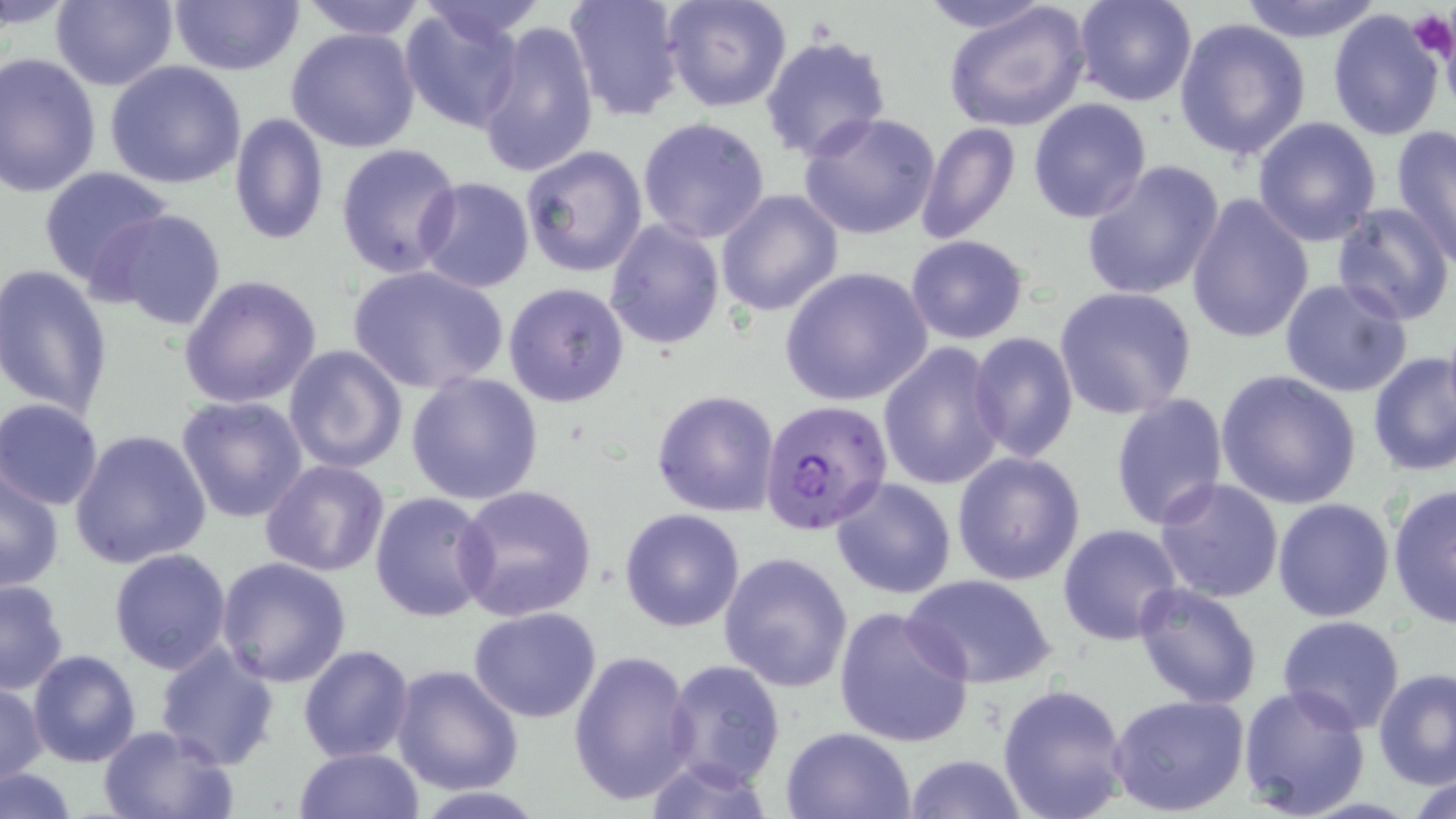

slide_level_diagnosis: Plasmodium falciparum
uninfected_red_blood_cell_locations: 'approximate bounding boxes as [x1, y1, x2, y2] in pixels: [52, 0, 178, 91], [294, 0, 432, 42], [415, 0, 549, 42], [563, 0, 687, 122], [662, 0, 793, 113], [912, 0, 1057, 36], [1074, 0, 1198, 107], [1235, 0, 1385, 40], [168, 1, 305, 76], [944, 2, 1091, 134], [398, 4, 527, 133], [1327, 7, 1447, 141], [476, 18, 599, 178], [1173, 18, 1313, 162], [287, 27, 420, 154], [760, 34, 890, 161], [0, 51, 102, 199], [104, 60, 247, 191], [1027, 98, 1152, 223], [228, 111, 331, 245], [799, 112, 942, 241], [636, 117, 771, 245], [1253, 117, 1383, 246], [916, 120, 1021, 247], [1390, 123, 1456, 265], [335, 143, 461, 278], [520, 145, 649, 277], [1081, 160, 1226, 303], [38, 165, 174, 294], [415, 178, 535, 293], [715, 188, 843, 317], [1185, 193, 1314, 344], [1330, 200, 1456, 326], [94, 208, 230, 334], [604, 219, 725, 352], [905, 234, 1031, 345], [347, 264, 510, 395], [0, 265, 115, 419], [777, 265, 934, 408], [177, 274, 322, 411], [1279, 278, 1412, 397], [503, 282, 631, 409], [1054, 287, 1198, 418], [969, 331, 1079, 466], [877, 343, 1006, 492], [282, 345, 408, 473], [1368, 351, 1454, 479], [1217, 370, 1361, 508], [405, 371, 545, 505], [651, 391, 779, 518], [1109, 393, 1229, 531], [177, 396, 308, 522], [0, 399, 103, 510], [0, 405, 191, 528], [70, 429, 211, 569], [951, 452, 1086, 585], [259, 459, 389, 578], [1, 468, 65, 593], [831, 477, 957, 601], [1153, 478, 1284, 603], [1387, 483, 1455, 631], [454, 485, 597, 622], [369, 491, 497, 625], [1273, 497, 1395, 621], [619, 508, 746, 631], [1058, 524, 1183, 645], [109, 549, 233, 675], [719, 551, 855, 692], [214, 556, 352, 686], [902, 574, 1057, 688], [0, 579, 70, 696], [1132, 584, 1263, 710], [832, 606, 974, 748], [468, 607, 602, 723], [1276, 616, 1406, 735], [153, 643, 281, 770], [298, 644, 415, 764], [568, 649, 696, 807], [27, 650, 141, 767], [661, 658, 787, 791], [391, 662, 524, 796], [1372, 668, 1456, 790], [0, 683, 46, 788], [996, 683, 1132, 819], [1238, 684, 1370, 817], [1109, 692, 1251, 816], [97, 725, 236, 819], [779, 725, 917, 818], [294, 744, 423, 819], [904, 752, 1028, 819], [643, 756, 778, 818], [1, 768, 77, 819], [1407, 771, 1455, 817]'
platelet_locations: 'approximate bounding boxes as [x1, y1, x2, y2] in pixels: [1405, 10, 1455, 62]'
stain: May-Grünwald-Giemsa
magnification: 1000x
image_size: 1456×819 pixels
field_of_view: single
modality: optical microscopy
plasmodium_falciparum_infected_red_blood_cell_locations: 'approximate bounding boxes as [x1, y1, x2, y2] in pixels: [768, 407, 903, 540]'
preparation: thin blood smear